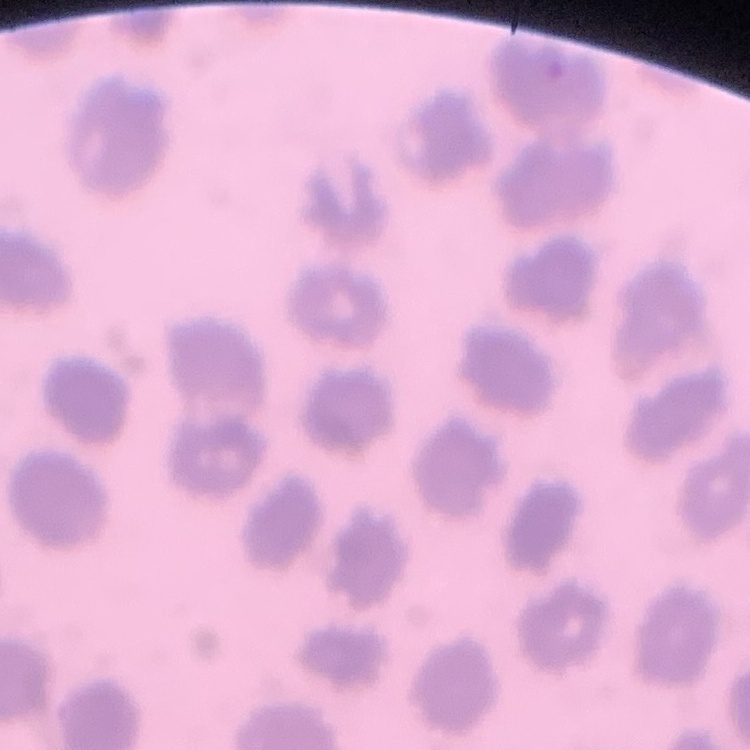
The red blood cells exhibit no rouleaux formation. Square crop of a larger photomicrograph. Field's or Giemsa stain. Thin peripheral smear.